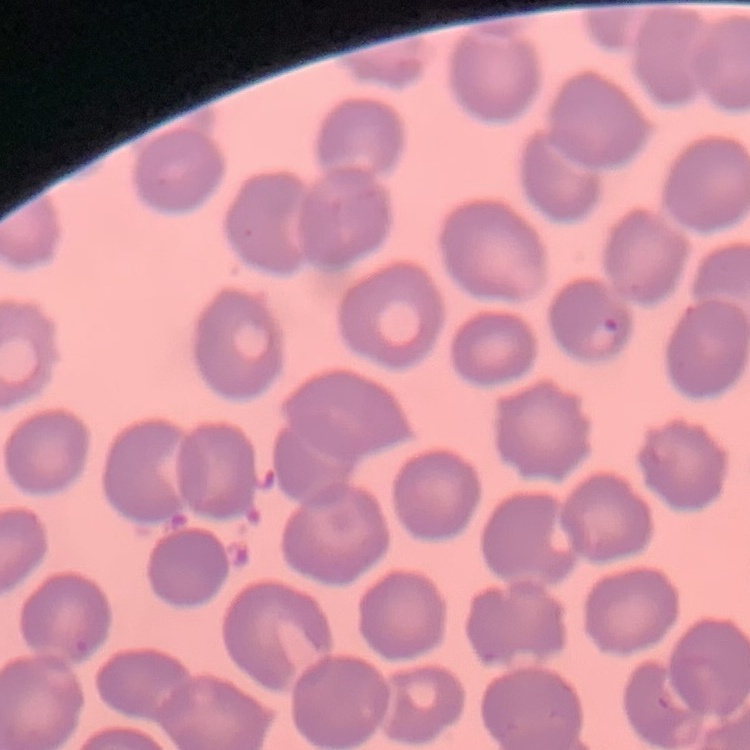

The erythrocytes show no rouleaux formation. Stained with either Field's or Giemsa. One tile cut from a larger photomicrograph. Thin blood smear.